Outline each Plasmodium malariae-infected red blood cell.
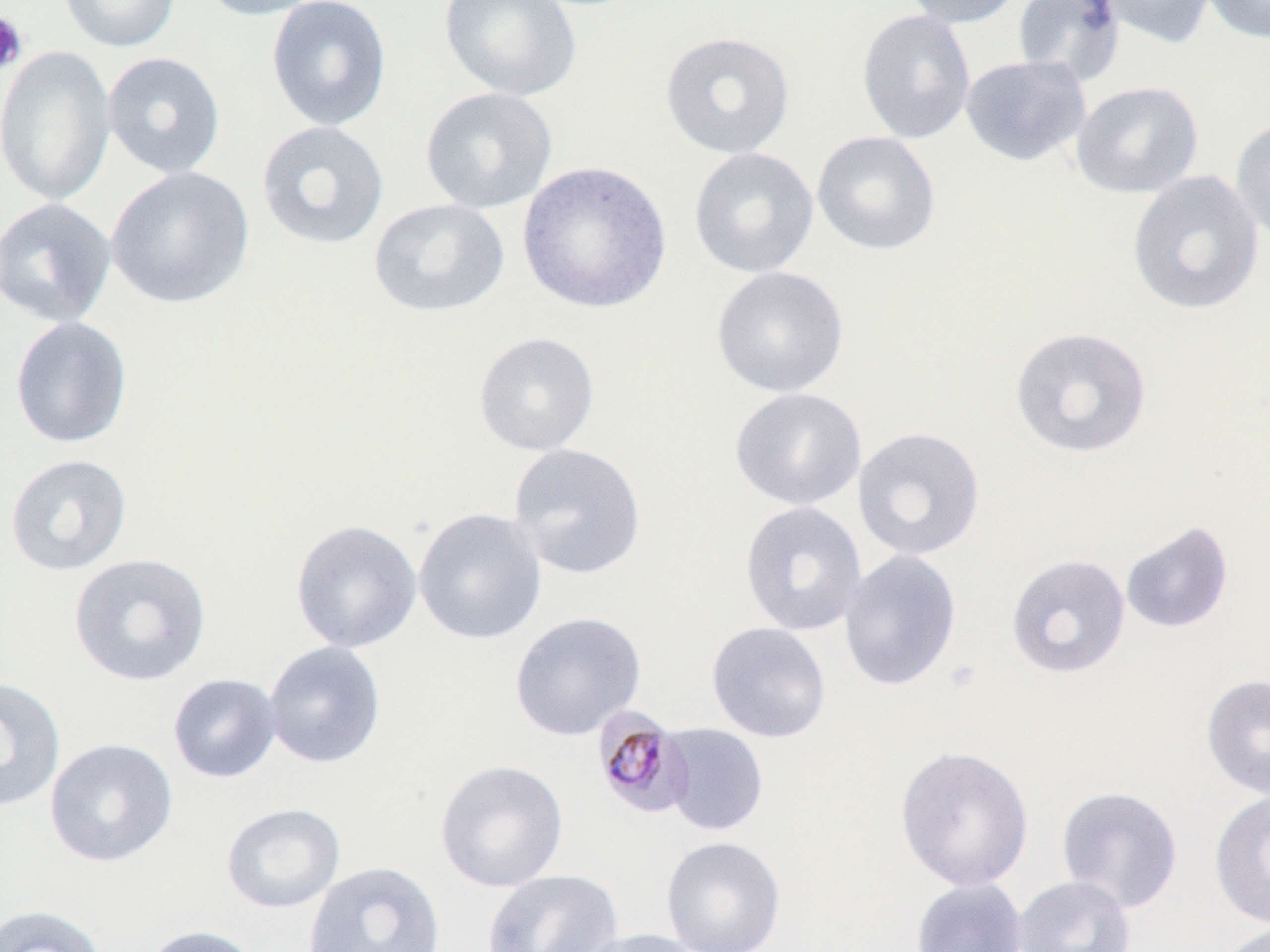

Approximate bounding boxes as (x1, y1, x2, y2) in pixels.
Plasmodium malariae-infected red blood cells: (591, 705, 693, 820).

Platelet locations: (0, 12, 29, 75). Uninfected red blood cell locations: (58, 0, 181, 53), (195, 0, 330, 21), (266, 0, 392, 132), (438, 0, 582, 102), (900, 0, 1022, 28), (1012, 0, 1125, 86), (1093, 0, 1217, 49), (1201, 0, 1270, 44), (856, 8, 976, 144), (660, 30, 796, 159), (0, 44, 117, 206), (102, 51, 226, 179), (960, 53, 1091, 167), (1071, 81, 1204, 198), (419, 87, 558, 215), (1230, 117, 1270, 245), (255, 120, 390, 251), (811, 130, 941, 256), (688, 146, 820, 279), (517, 160, 672, 315), (105, 166, 255, 310), (1127, 169, 1265, 316), (0, 197, 117, 328), (369, 198, 510, 318), (711, 265, 850, 397), (9, 316, 133, 449), (1009, 326, 1152, 459), (473, 330, 600, 456), (729, 387, 867, 511), (852, 426, 986, 562), (508, 442, 647, 580), (4, 453, 133, 577), (739, 500, 868, 637), (413, 507, 547, 645), (290, 518, 422, 654), (1119, 520, 1235, 635), (837, 549, 962, 692), (68, 552, 212, 687), (1005, 553, 1131, 679), (509, 611, 646, 742), (706, 621, 832, 743), (263, 641, 386, 768), (168, 673, 282, 783), (1201, 673, 1270, 800), (0, 676, 67, 813), (660, 722, 769, 837), (45, 738, 178, 867), (894, 745, 1034, 892), (434, 758, 569, 892), (1055, 785, 1183, 914), (1209, 789, 1270, 930), (221, 803, 346, 913), (660, 836, 786, 952), (303, 860, 445, 952), (481, 868, 624, 952), (1012, 874, 1136, 952), (910, 877, 1029, 952), (0, 904, 108, 952), (1214, 921, 1269, 952), (141, 924, 261, 952), (577, 927, 708, 952). Slide-level diagnosis: Plasmodium malariae. May-Grünwald-Giemsa stain. 1000x magnification. Image is 1270×952 pixels. Optical microscopy. Thin blood smear. One field of a larger specimen.